Identify the parasite.
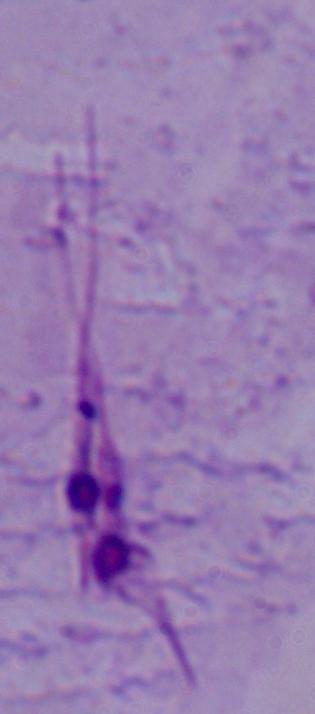
This is Leishmania.

Summary:
  - Magnification: 1000x
  - Modality: photomicrograph